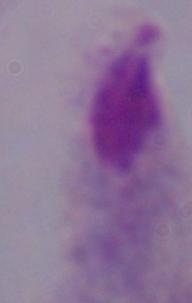 1000x magnification. Micrograph. A trichomonad is shown.